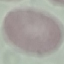
Summary:
  - Malaria status: uninfected
  - Preparation: thin blood film
  - Capture: smartphone camera at the microscope eyepiece
  - Image type: cell patch, automatically extracted from a larger field of view and resized to 64 × 64 pixels
  - Stain: Giemsa